Locate every malaria parasite and every leukocyte.
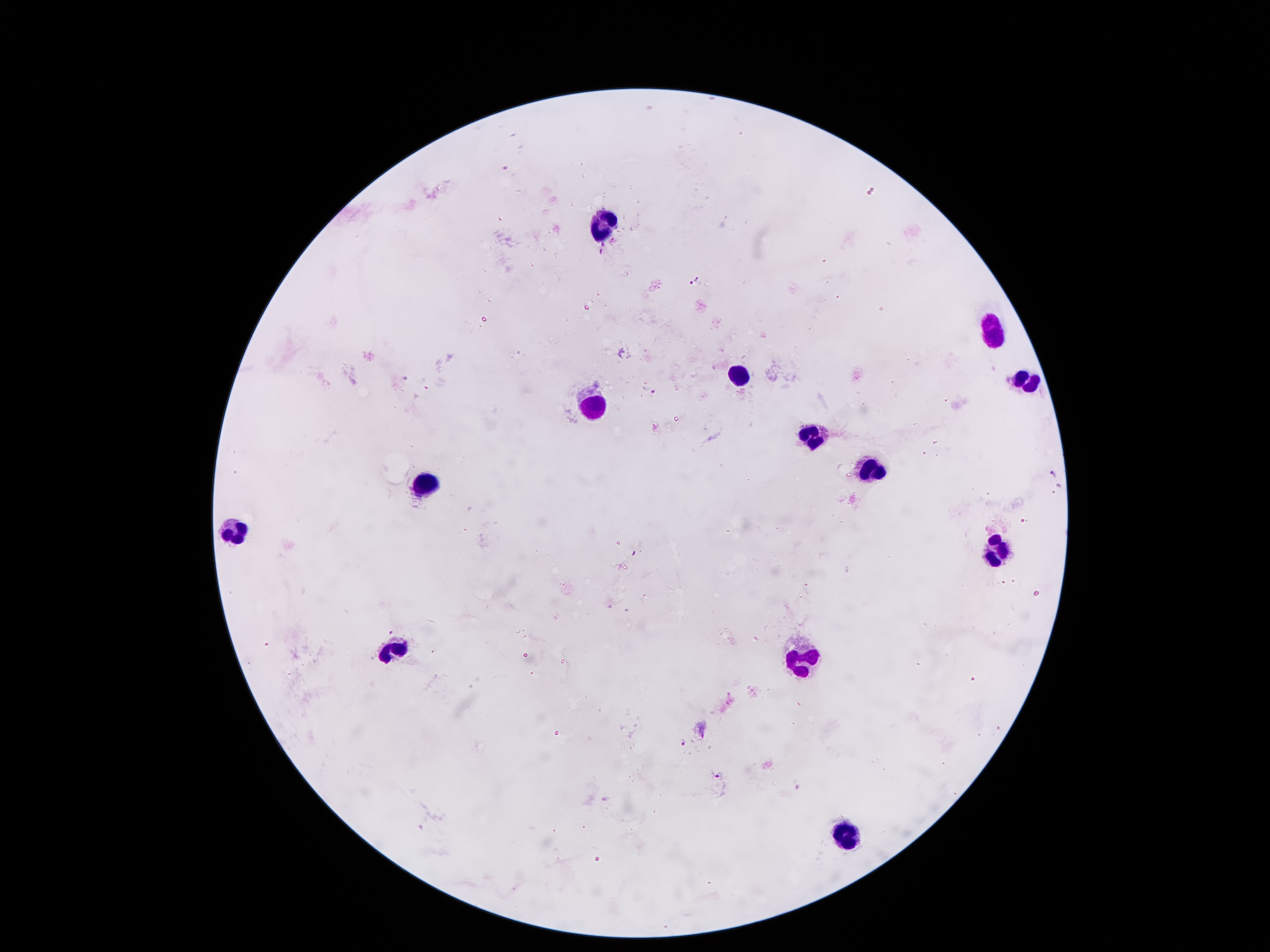

Approximate centers as (x, y) in pixels.
Malaria parasites: (694, 281), (405, 378), (649, 389), (683, 742), (718, 776).
Leukocytes: (598, 227), (996, 333), (737, 378), (1028, 381), (594, 406), (814, 436), (876, 469), (428, 486), (235, 531), (994, 549), (398, 650), (805, 658), (846, 833).

stain = Giemsa
field of view = single
image size = 1270×952 pixels
preparation = thick blood smear
patient malaria status = positive for Plasmodium falciparum
capture = smartphone through the microscope eyepiece
magnification = 100x